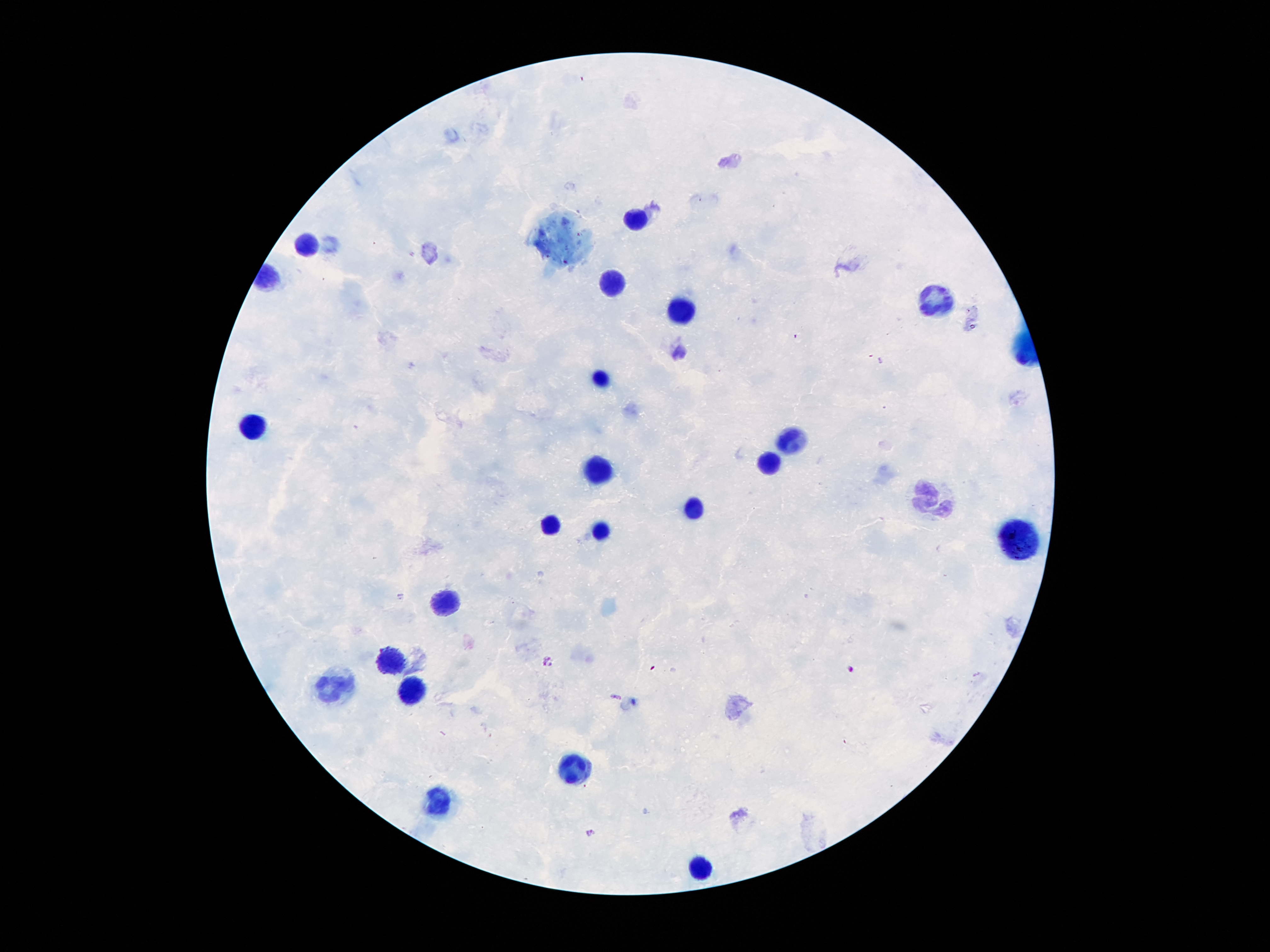

coordinate format = approximate centers as (x, y) in pixels
leukocyte locations = (634, 220), (304, 245), (612, 281), (931, 299), (679, 313), (597, 379), (253, 424), (790, 437), (768, 461), (595, 468), (931, 499), (691, 509), (553, 526), (597, 533), (1017, 538), (436, 602), (385, 659), (338, 689), (409, 694), (577, 767), (439, 800), (698, 869)
Plasmodium parasite locations = (548, 663), (850, 669), (591, 831)
preparation = thick blood film
image size = 1270×952 pixels
field of view = one from this slide
patient malaria status = infected with Plasmodium falciparum
magnification = 100x
capture = smartphone through the microscope eyepiece
stain = Giemsa